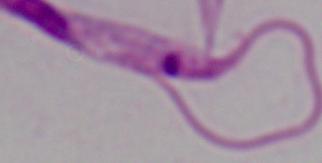 Captured at 1000x magnification. Photomicrograph. A Leishmania parasite is shown.